Assess this cell for malaria.
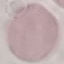

Uninfected.

capture = smartphone camera at the microscope eyepiece
preparation = thin smear
stain = Giemsa
image type = automatically extracted cell patch, resized to 64 × 64 pixels